Comment on the morphology of the red blood cells.
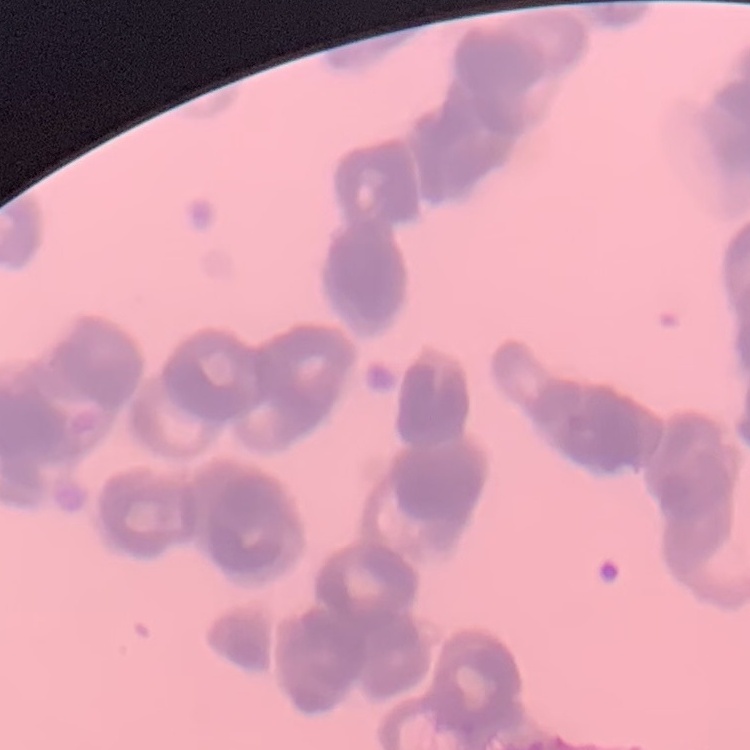

They show rouleaux formation.

Summary:
  - Image type: square crop of a larger photomicrograph
  - Preparation: thin peripheral smear
  - Stain: Field's or Giemsa